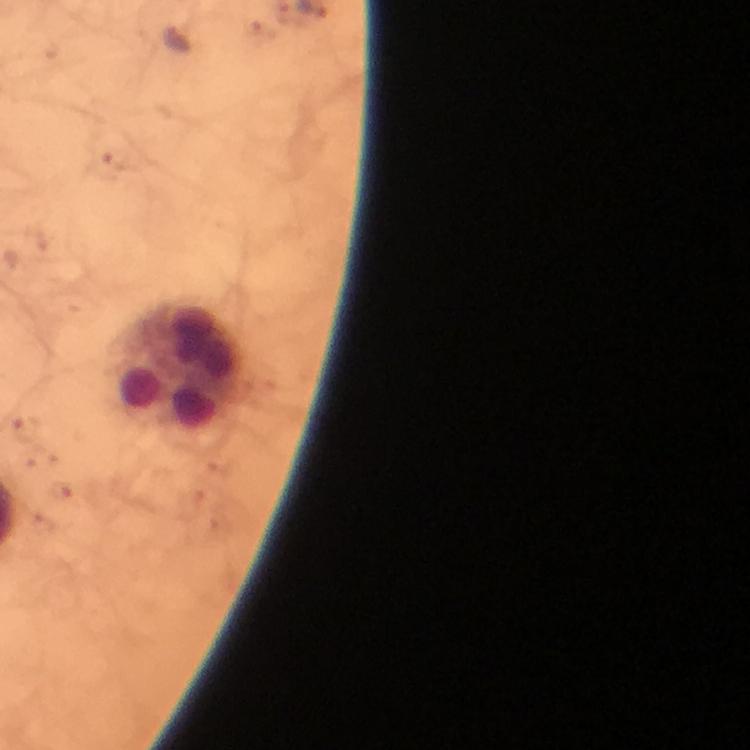
{
  "context": "from a malaria diagnostic workup",
  "malaria_parasite_locations": "approximate centers as (x, y) in pixels: (178, 39), (118, 160), (25, 430)",
  "cropped_from": "one field of view",
  "magnification": "100x",
  "stain": "Giemsa",
  "image_size": "750×750 pixels",
  "preparation": "thick blood film",
  "capture": "smartphone camera through the microscope",
  "leukocyte_locations": "approximate centers as (x, y) in pixels: (175, 370)",
  "immersion_oil": "applied"
}